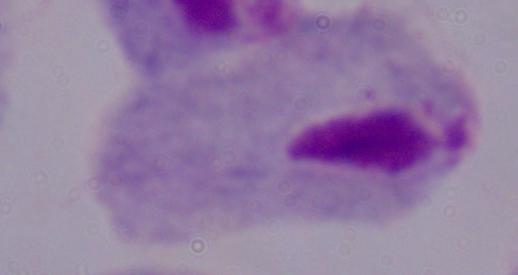

magnification = 1000x
identification = trichomonad
modality = micrograph